Locate every blood parasite and identify its species.
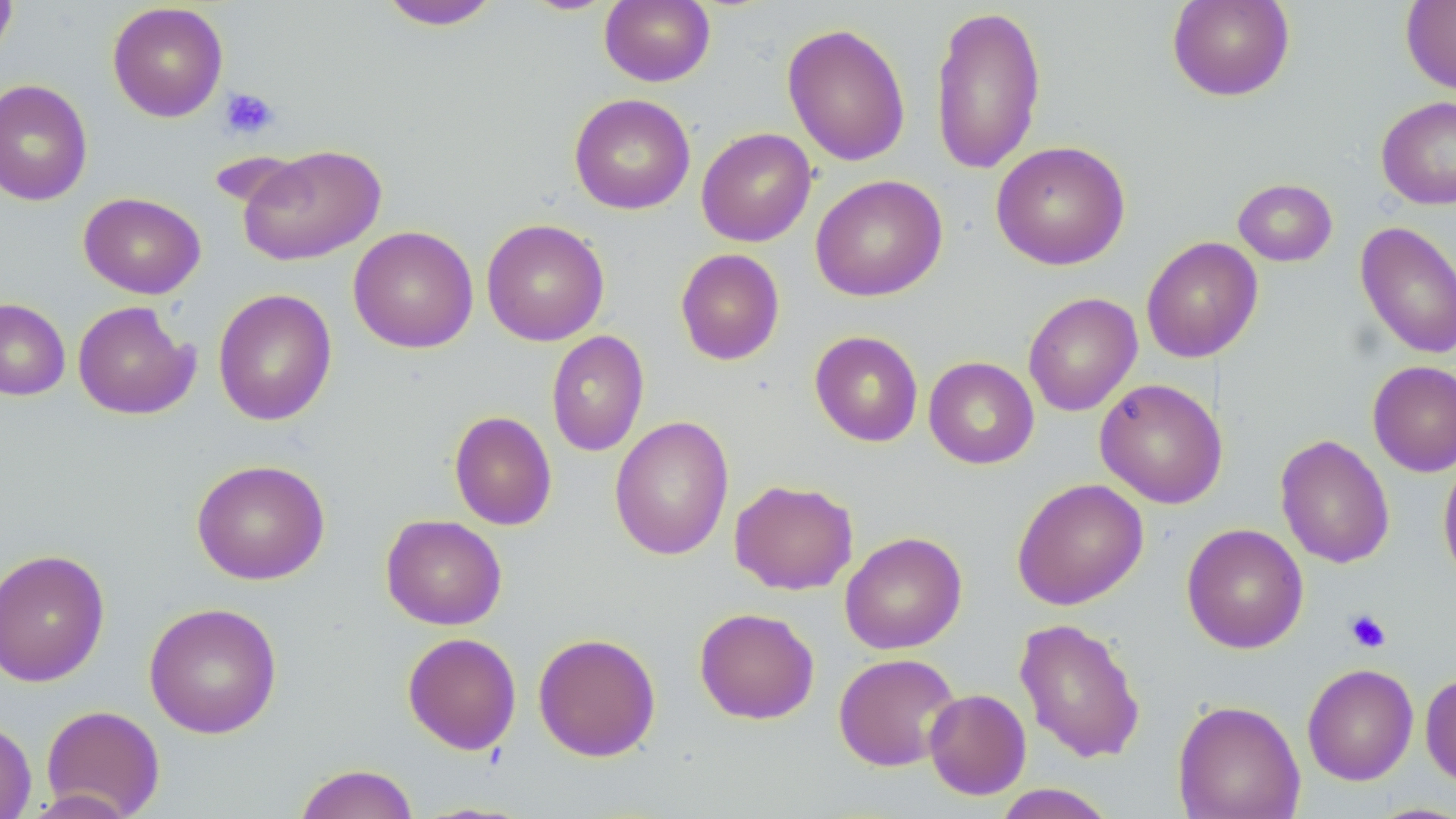

No blood parasites observed.

Approximate bounding boxes as [x1, y1, x2, y2] in pixels. Uninfected red blood cell locations: [0, 0, 18, 63], [599, 0, 716, 87], [1167, 0, 1295, 101], [1401, 0, 1456, 95], [377, 1, 503, 30], [107, 2, 228, 122], [930, 4, 1047, 174], [782, 22, 911, 167], [0, 79, 92, 206], [568, 93, 696, 215], [1376, 95, 1456, 210], [696, 127, 816, 247], [991, 140, 1130, 270], [237, 144, 387, 266], [810, 174, 948, 302], [1232, 178, 1338, 267], [78, 192, 206, 299], [481, 218, 610, 346], [1355, 220, 1456, 360], [348, 225, 478, 353], [1140, 236, 1264, 363], [675, 248, 785, 365], [213, 288, 337, 426], [1023, 292, 1142, 416], [0, 298, 70, 400], [72, 300, 199, 420], [546, 330, 649, 457], [810, 331, 923, 447], [923, 356, 1039, 469], [1367, 360, 1456, 477], [1094, 378, 1228, 509], [449, 410, 557, 530], [609, 415, 734, 560], [1275, 434, 1395, 569], [1438, 455, 1456, 585], [191, 458, 330, 585], [1011, 478, 1149, 610], [729, 479, 858, 595], [381, 514, 507, 630], [1181, 523, 1309, 654], [840, 532, 967, 654], [0, 548, 111, 686], [143, 602, 283, 738], [694, 607, 819, 724], [1014, 617, 1146, 763], [402, 632, 521, 754], [533, 632, 661, 762], [833, 652, 961, 771], [1302, 663, 1418, 785], [1420, 672, 1456, 787], [923, 688, 1031, 800], [1173, 699, 1305, 819], [41, 704, 165, 818], [0, 718, 37, 819], [294, 763, 419, 819], [990, 784, 1119, 818]. Platelet locations: [220, 86, 280, 140], [1344, 608, 1391, 653]. Slide-level diagnosis: negative for blood parasites. May-Grünwald-Giemsa stain. Thin blood smear. One field of a larger specimen. Image is 1456×819 pixels. Captured at 1000x magnification. Optical microscopy.